Classify this cell by malaria status.
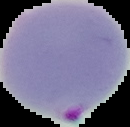
Parasitized.

{
  "image_size": "130×127 pixels",
  "image_type": "cell region segmented out of the field of view; surrounding area masked to black",
  "preparation": "thin blood film"
}